Report the malaria status of this cell.
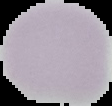
Uninfected.

Summary:
  - Image size: 112×106 pixels
  - Preparation: thin blood smear
  - Image type: cell region segmented out of the field of view; surrounding area masked to black